Outline every parasitised red blood cell.
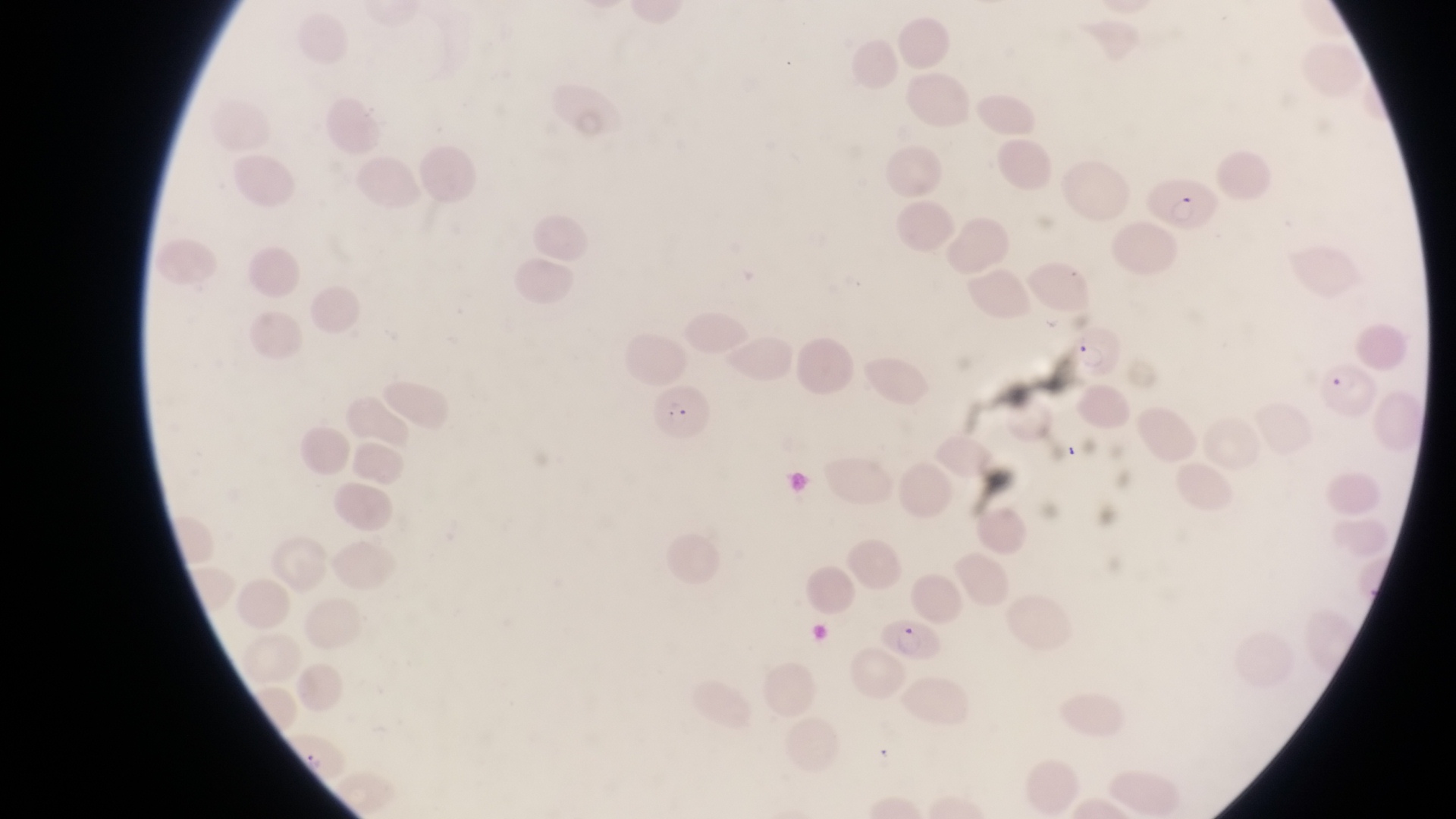

Approximate bounding boxes as [left, top, right, bottom] in pixels.
Parasitised red blood cells: [1155, 172, 1215, 232], [1067, 323, 1125, 381], [1321, 360, 1374, 415], [653, 381, 709, 441], [878, 616, 944, 668].

Summary:
  - Country: Uganda
  - Image size: 1456×819 pixels
  - Field of view: single
  - Capture: smartphone photograph through the eyepiece of an Olympus CX-23 microscope
  - Preparation: thin blood film
  - Magnification: 1000x